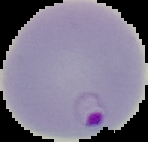 Image is 148×142 pixels. Malaria status: parasitized. From a thin blood smear. The area outside the segmented cell region is set to black.